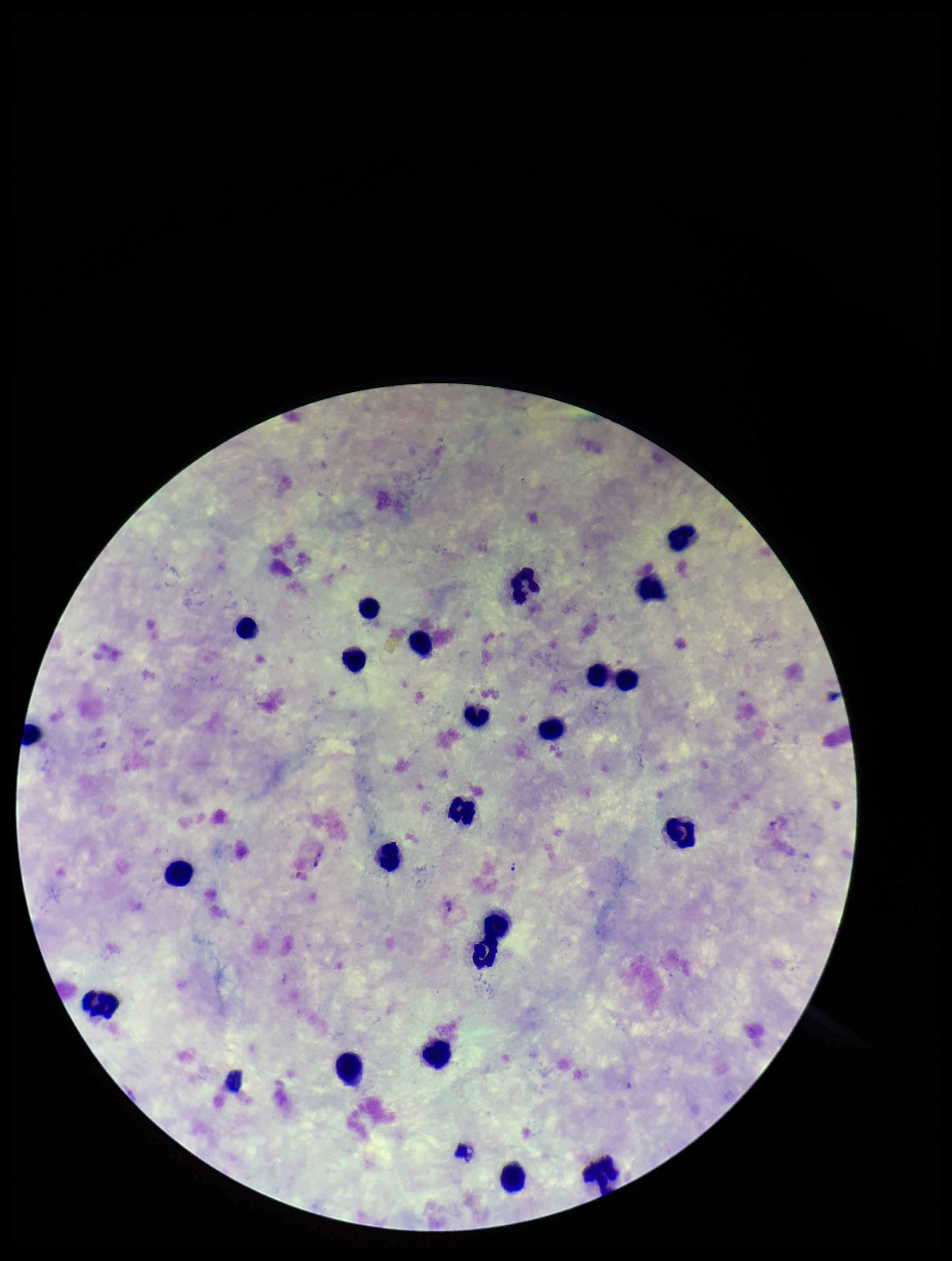

Summary:
  - Preparation: thick blood smear
  - Leukocyte count: 23
  - Plasmodium parasites: seen
  - Patient malaria status: infected
  - Field of view: single
  - Parasite count: 1
  - Image size: 952×1261 pixels
  - Species reported for this patient: Plasmodium vivax
  - Stain: Giemsa
  - Capture: smartphone photograph through the microscope eyepiece